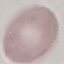

Malaria status: uninfected. Giemsa stain. Photographed with a smartphone camera at the microscope eyepiece. Automatically extracted cell patch, resized to 64 × 64 pixels. Thin blood film.